Locate every uninfected red blood cell.
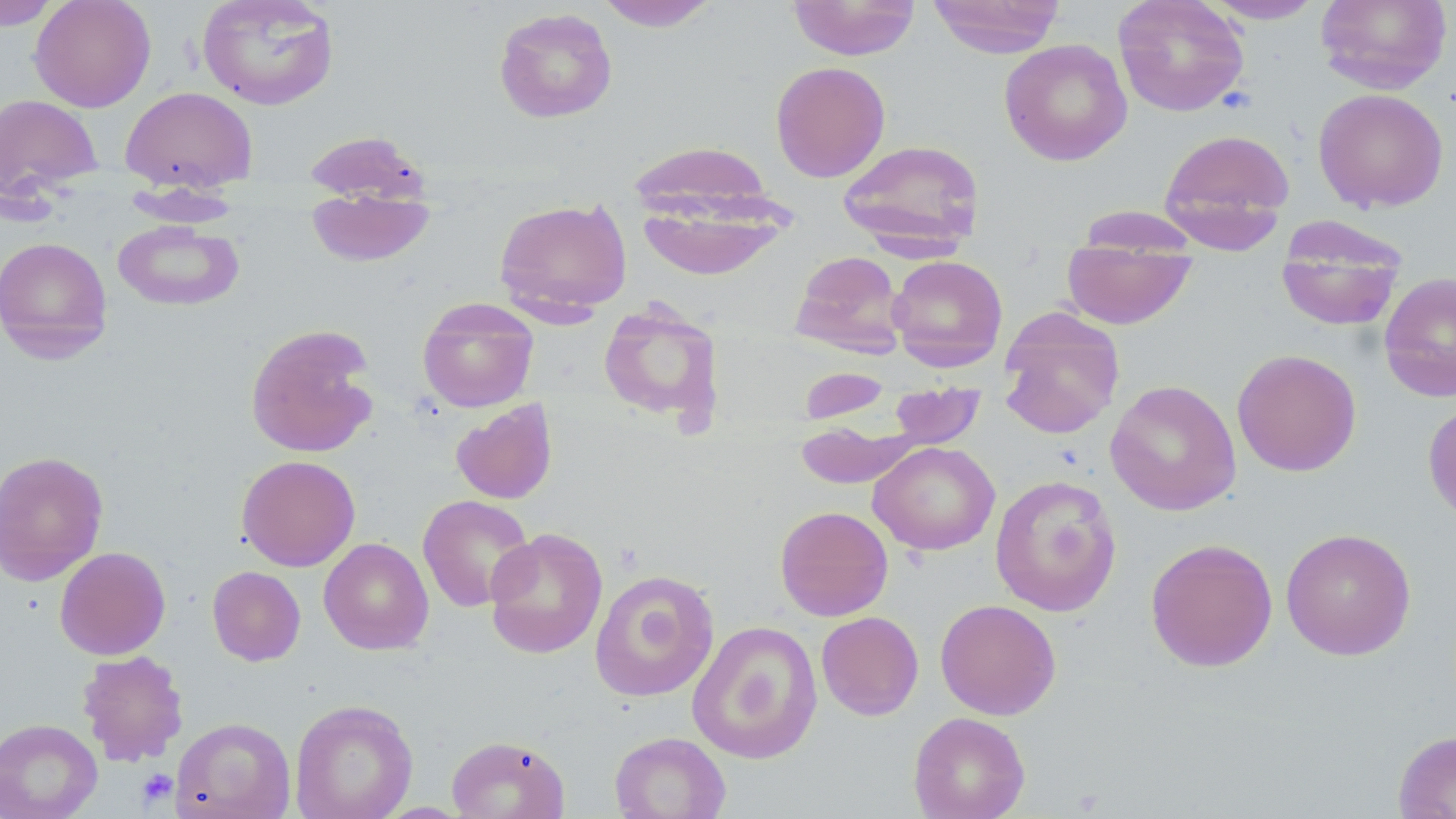

Approximate bounding boxes as (x1, y1, x2, y2) in pixels.
Uninfected red blood cells: (0, 0, 62, 29), (29, 0, 156, 112), (196, 0, 340, 110), (594, 0, 721, 31), (787, 0, 921, 60), (927, 0, 1066, 57), (1113, 0, 1249, 117), (1201, 0, 1328, 24), (1315, 0, 1452, 94), (493, 7, 617, 123), (999, 38, 1132, 166), (770, 61, 890, 183), (120, 86, 258, 194), (1313, 88, 1449, 213), (0, 93, 103, 203), (1159, 128, 1296, 250), (302, 130, 430, 206), (627, 139, 782, 231), (838, 139, 985, 254), (630, 163, 794, 279), (123, 183, 242, 226), (306, 189, 435, 267), (493, 197, 633, 320), (1075, 205, 1201, 254), (113, 219, 244, 312), (1275, 221, 1407, 332), (0, 236, 113, 362), (1062, 242, 1198, 329), (790, 250, 907, 358), (887, 255, 1008, 371), (1379, 272, 1456, 402), (417, 297, 539, 413), (598, 302, 725, 427), (998, 309, 1124, 439), (245, 323, 380, 459), (1232, 348, 1362, 476), (797, 367, 892, 424), (1105, 379, 1241, 516), (888, 381, 985, 449), (1422, 397, 1456, 527), (450, 398, 558, 505), (794, 421, 920, 489), (869, 441, 1000, 555), (0, 449, 109, 586), (236, 454, 360, 571), (990, 474, 1122, 617), (418, 494, 535, 612), (775, 505, 893, 621), (484, 527, 608, 659), (1280, 527, 1417, 660), (319, 537, 433, 655), (1145, 537, 1278, 672), (54, 546, 171, 659), (207, 566, 306, 666), (590, 570, 720, 702), (935, 598, 1061, 720), (816, 611, 924, 721), (687, 620, 823, 764), (77, 649, 189, 767), (290, 699, 418, 819), (908, 711, 1031, 819), (171, 717, 296, 819), (0, 718, 103, 819), (1393, 729, 1456, 819), (609, 731, 731, 819), (446, 735, 570, 819).

{
  "slide_level_diagnosis": "negative for blood parasites",
  "stain": "May-Grünwald-Giemsa",
  "field_of_view": "one of a larger specimen",
  "image_size": "1456×819 pixels",
  "preparation": "thin blood smear",
  "modality": "optical microscopy",
  "magnification": "1000x",
  "platelet_locations": "approximate bounding boxes as (x1, y1, x2, y2) in pixels: (136, 768, 178, 808)"
}